Identify the blood parasite species.
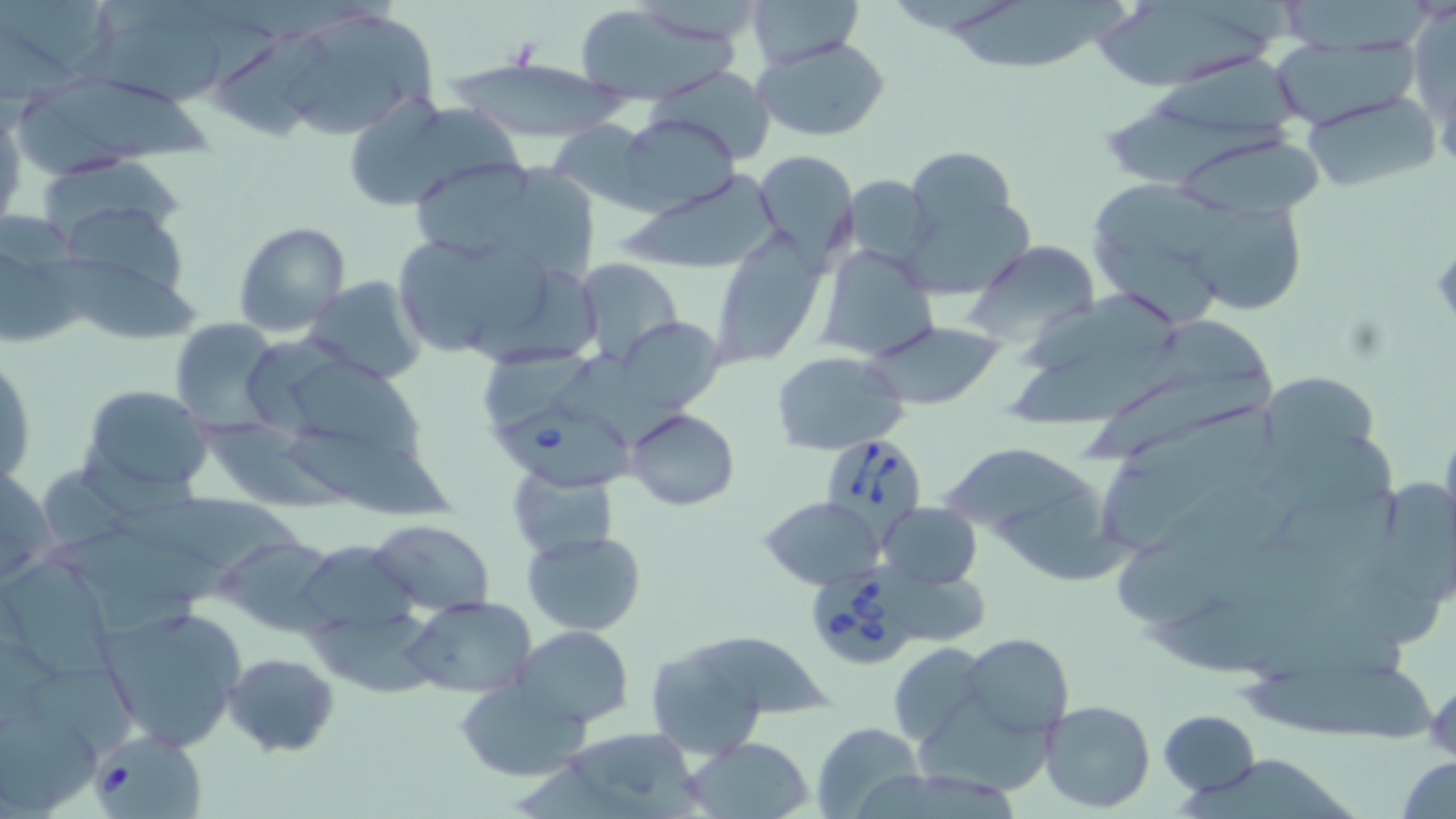
Babesia divergens.

Approximate bounding boxes as (x1, y1, x2, y2) in pixels. Uninfected red blood cell locations: (0, 0, 105, 78), (748, 0, 867, 67), (1286, 0, 1431, 54), (953, 2, 1130, 71), (1090, 2, 1279, 88), (571, 3, 739, 105), (274, 7, 438, 143), (1414, 10, 1456, 126), (87, 24, 230, 110), (220, 29, 334, 141), (753, 34, 891, 142), (1265, 38, 1418, 128), (450, 57, 624, 141), (646, 66, 777, 160), (18, 73, 214, 171), (1299, 92, 1439, 194), (340, 93, 511, 213), (0, 102, 26, 231), (1109, 104, 1297, 187), (617, 112, 739, 217), (546, 121, 653, 213), (1170, 127, 1325, 222), (906, 146, 1018, 238), (755, 150, 857, 265), (41, 153, 188, 244), (418, 161, 535, 256), (497, 165, 600, 283), (624, 170, 784, 273), (843, 175, 937, 263), (1091, 177, 1240, 264), (58, 200, 190, 299), (1197, 203, 1314, 314), (899, 206, 1033, 300), (232, 221, 352, 336), (0, 225, 85, 349), (387, 231, 557, 359), (711, 231, 827, 367), (966, 243, 1101, 345), (1092, 244, 1219, 324), (817, 245, 942, 362), (36, 248, 203, 340), (576, 258, 683, 365), (302, 274, 429, 385), (1022, 290, 1183, 379), (1144, 316, 1274, 395), (168, 318, 284, 435), (622, 321, 735, 410), (866, 322, 1003, 409), (1011, 337, 1198, 428), (480, 342, 585, 424), (563, 349, 687, 445), (0, 350, 35, 489), (772, 351, 908, 455), (283, 355, 426, 460), (1085, 369, 1276, 466), (1259, 370, 1383, 467), (80, 385, 214, 495), (626, 409, 740, 511), (194, 415, 353, 512), (284, 418, 457, 517), (1248, 431, 1394, 512), (945, 446, 1095, 536), (0, 461, 56, 587), (1095, 461, 1221, 542), (508, 464, 618, 561), (41, 465, 132, 555), (1387, 481, 1456, 611), (1275, 483, 1404, 570), (1000, 484, 1136, 582), (110, 494, 306, 576), (760, 496, 885, 590), (878, 502, 982, 589), (367, 519, 495, 615), (1112, 529, 1224, 624), (523, 530, 646, 635), (48, 532, 250, 601), (218, 536, 339, 634), (291, 541, 424, 652), (1, 560, 116, 678), (404, 596, 537, 699), (96, 603, 245, 751), (310, 610, 444, 700), (513, 626, 633, 728), (692, 633, 835, 720), (962, 633, 1073, 738), (642, 639, 774, 759), (886, 642, 990, 746), (222, 651, 340, 758), (28, 665, 135, 758), (1234, 665, 1437, 743), (1426, 677, 1454, 762), (455, 679, 591, 781), (917, 694, 1060, 797), (1040, 700, 1155, 813), (0, 707, 102, 810), (1158, 709, 1259, 796), (810, 723, 926, 818), (569, 724, 707, 818), (687, 738, 814, 817), (515, 756, 635, 819), (1397, 756, 1456, 819), (1180, 760, 1365, 819), (863, 769, 1022, 819). Babesia divergens-infected red blood cell locations: (493, 398, 640, 498), (824, 437, 929, 550), (806, 563, 916, 669), (91, 732, 207, 819). May-Grünwald-Giemsa stain. Thin blood film. Optical microscopy. 1000x magnification. Single field of view. Image is 1456×819 pixels.